Assess the background quality.
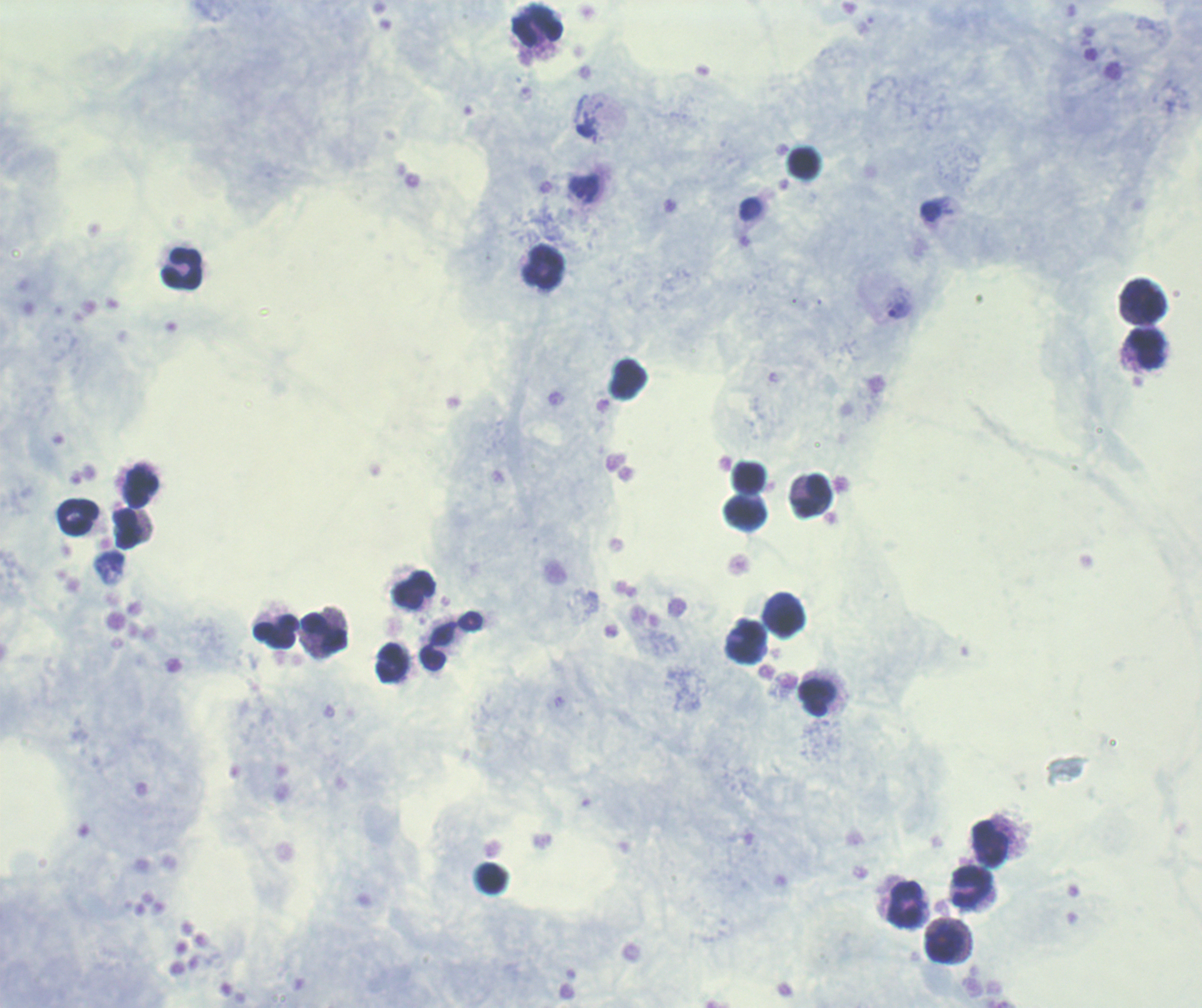
Satisfactory.

Approximate centers as [x, y] in pixels.
Summary:
  - Trophozoite locations: [583, 188], [899, 310]
  - Leukocyte locations: [538, 26], [545, 268], [182, 269], [1143, 300], [1146, 348], [749, 477], [140, 486], [813, 497], [746, 513], [78, 517], [128, 529], [414, 590], [789, 619], [276, 631], [324, 633], [746, 642], [438, 647], [392, 663], [817, 697], [990, 843], [972, 886], [905, 905], [946, 944]
  - Preparation: thick blood film
  - Coloration quality: good
  - Field of view: single
  - Stain: Romanowsky
  - Context: previously used in a real diagnosis
  - Result: positive for Plasmodium parasites
  - Image size: 1202×1008 pixels
  - Magnification: 100x